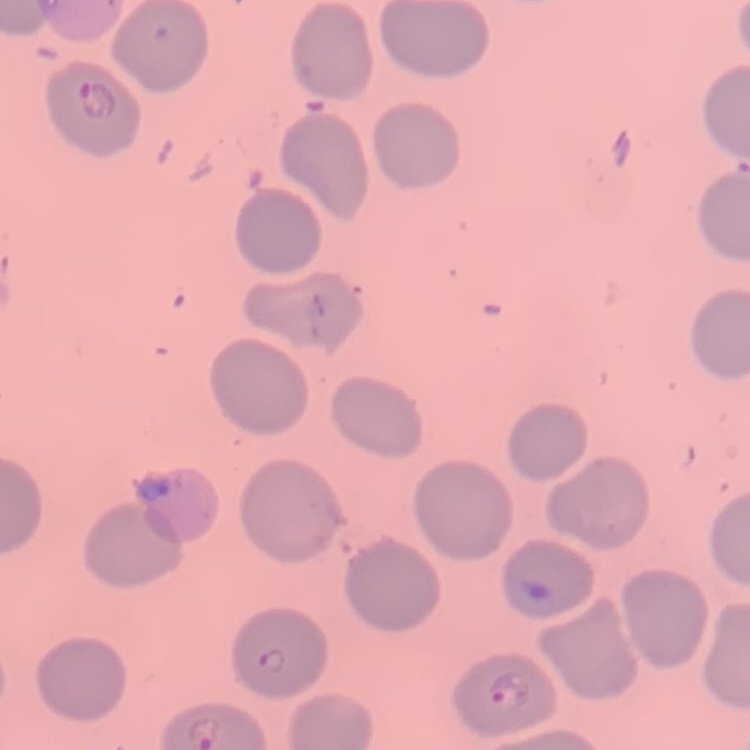

Summary:
  - Red blood cell morphology: no rouleaux formation
  - Image type: one tile cut from a larger photomicrograph
  - Stain: Field's or Giemsa
  - Preparation: thin blood film